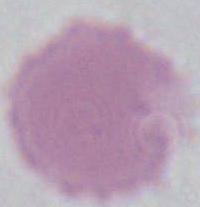 1000x magnification. An erythrocyte is shown. Photomicrograph.